Give the position of every malaria parasite.
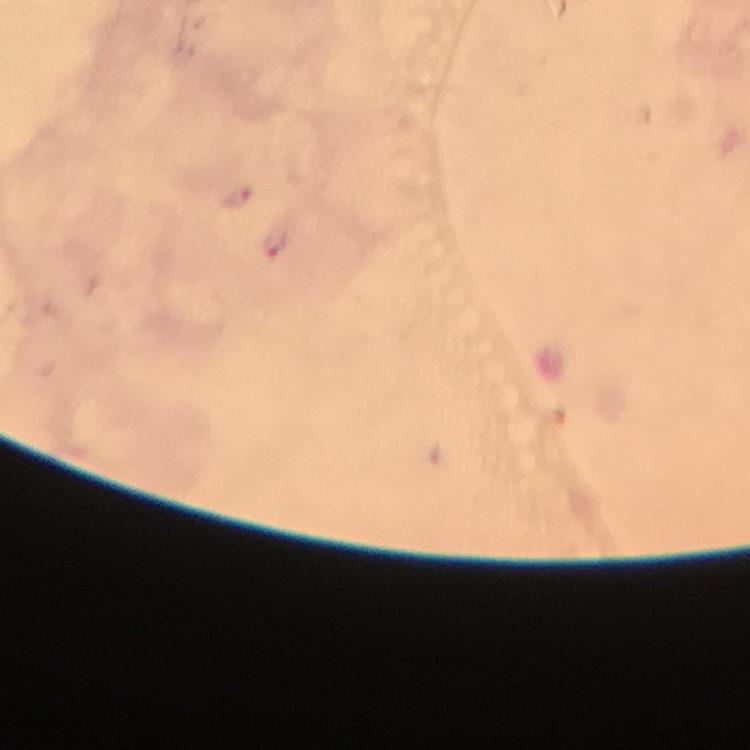
Approximate object centers, in pixels from the top-left corner.
Malaria parasites: (x=238, y=198), (x=278, y=241).

Summary:
  - Image size: 750×750 pixels
  - Capture: smartphone mounted on the microscope
  - Immersion oil: applied
  - Cropped from: one field of view
  - Stain: Giemsa
  - Preparation: thick blood smear
  - Context: from a malaria diagnostic workup
  - Magnification: 100x